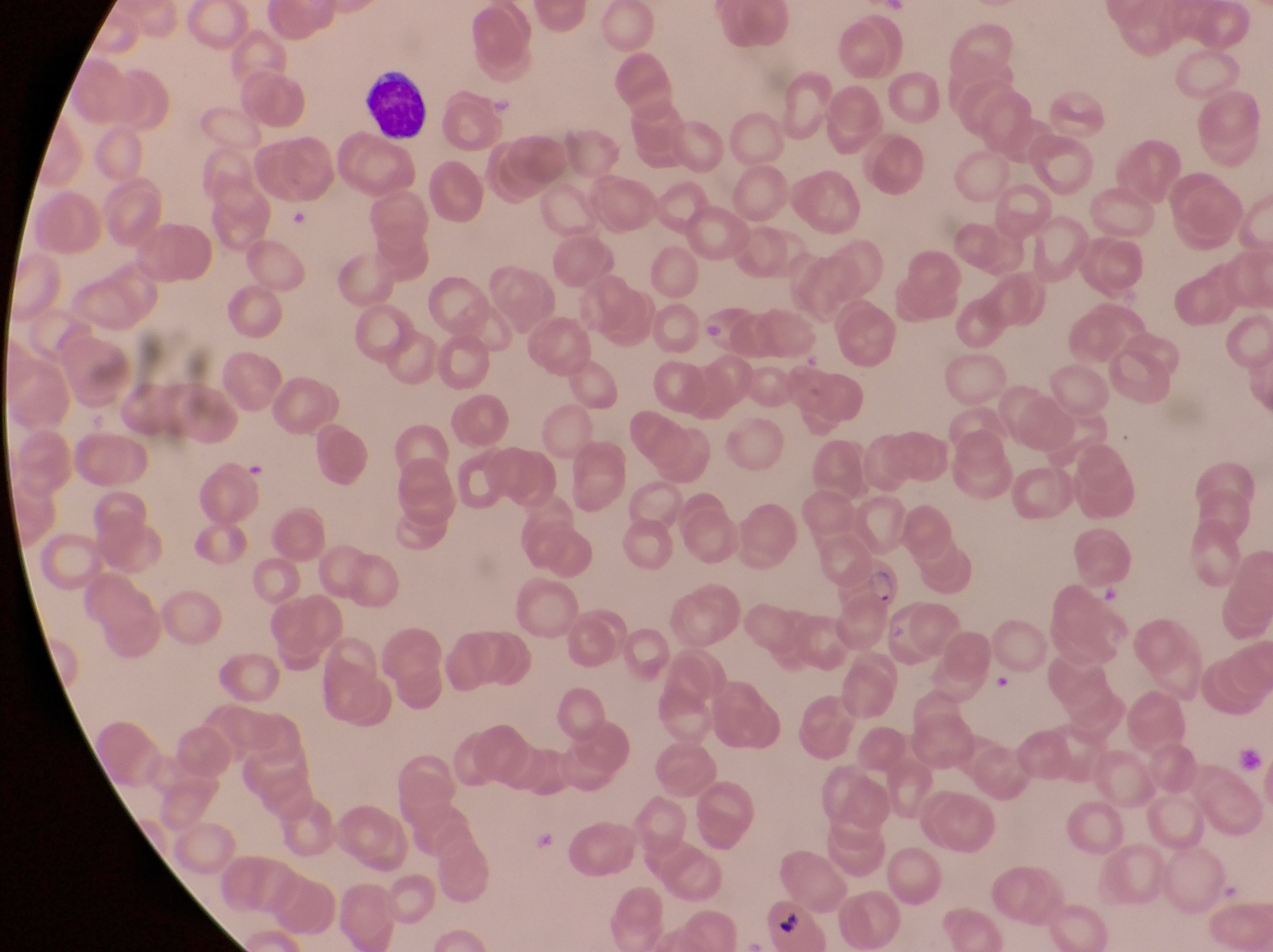
artifact (platelet-like body, stain precipitate, or debris) locations = approximate bounding boxes as {left, top, right, bottom} in pixels: {991, 671, 1014, 698}, {1237, 741, 1261, 772}
leukocyte locations = approximate bounding boxes as {left, top, right, bottom} in pixels: {354, 70, 429, 144}
country = Uganda
capture = smartphone photograph through the eyepiece of an Olympus CX-23 microscope
image size = 1273×952 pixels
magnification = 1000x
field of view = single
parasitised red blood cell locations = approximate bounding boxes as {left, top, right, bottom} in pixels: {843, 549, 906, 609}, {762, 897, 834, 944}
preparation = thin blood film